Describe the morphology of the red blood cells.
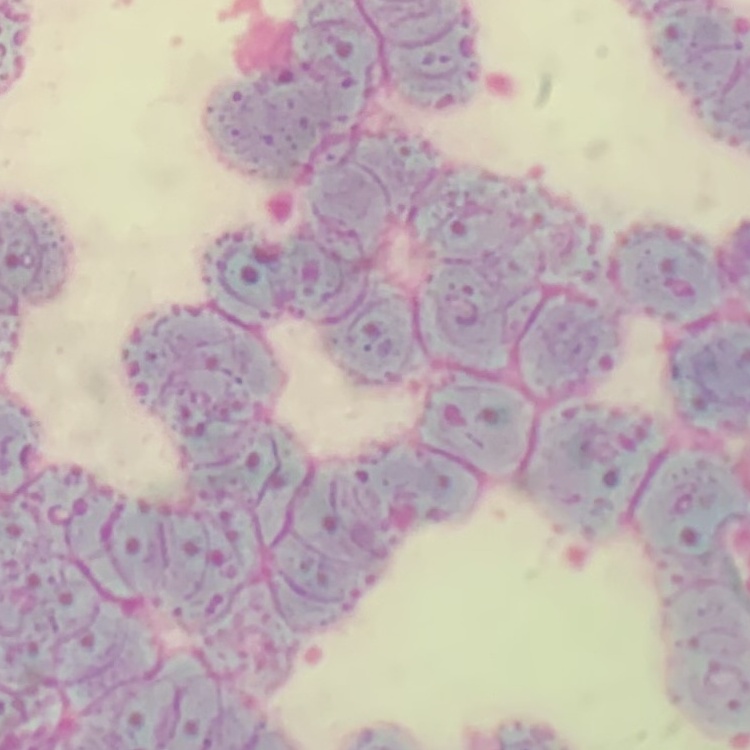

They show rouleaux formation.

{
  "preparation": "thin blood smear",
  "image_type": "one tile cut from a larger photomicrograph",
  "stain": "Field's or Giemsa"
}